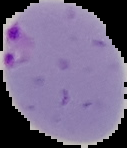
Result: malaria parasites identified. The area outside the segmented cell region is set to black. From a thin blood smear. Image is 127×148 pixels.